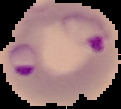
From a thin blood film. Segmented cell region on a black background. Image is 121×109 pixels. Malaria status: parasitized.